Assess this cell for malaria.
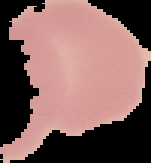

Uninfected.

image_size: 151×163 pixels
preparation: thin blood film
image_type: segmented cell region on a black background